Locate every white blood cell.
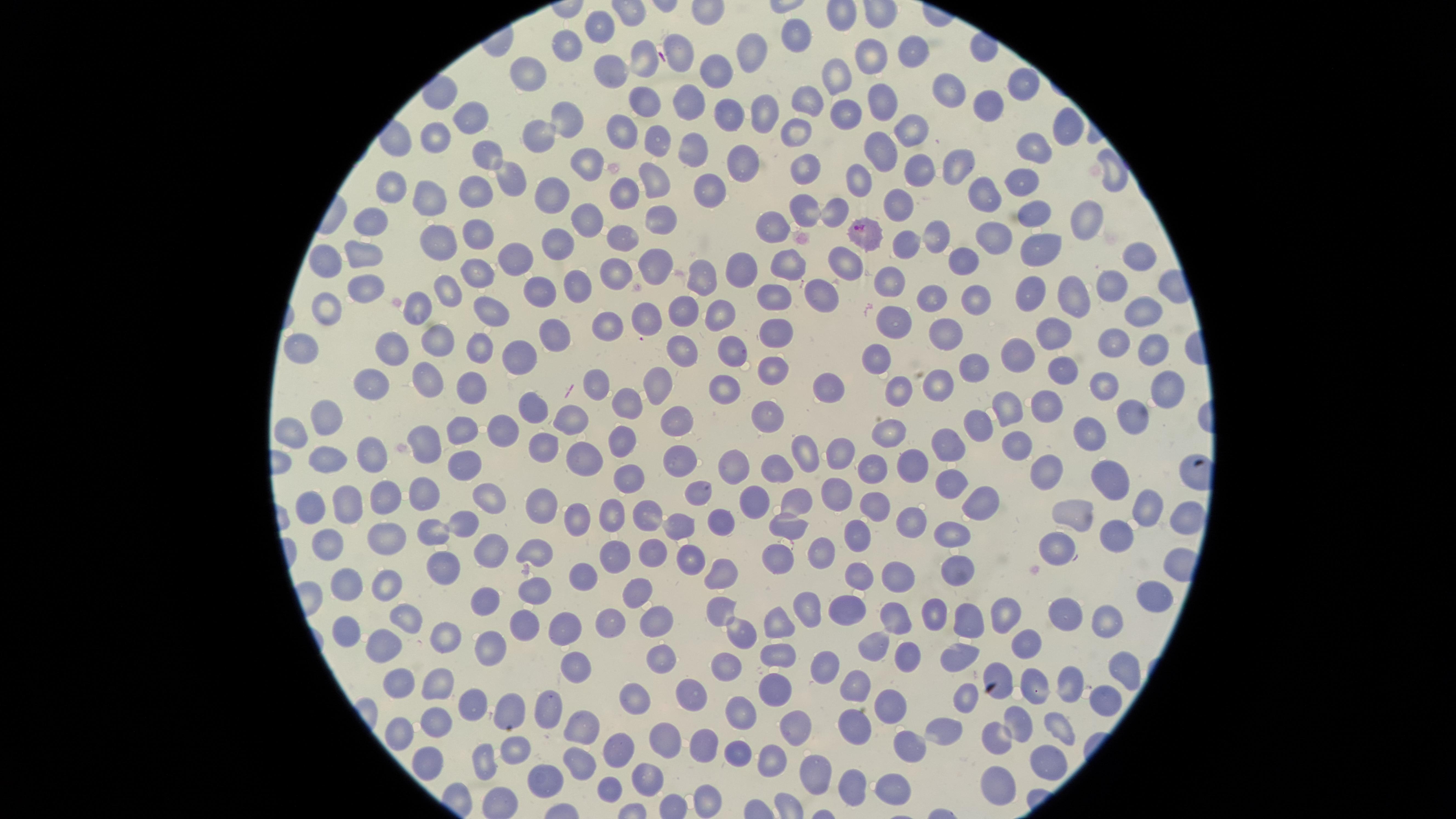
No white blood cells identified.

Approximate marker points as [x, y] in pixels.
Summary:
  - Parasitized red blood cells: [859, 230], [734, 351]
  - Uninfected red blood cells: [603, 29], [799, 32], [571, 44], [910, 50], [747, 54], [681, 55], [870, 55], [642, 57], [527, 69], [612, 70], [712, 72], [841, 73], [1020, 78], [954, 91], [806, 100], [644, 102], [888, 102], [688, 106], [764, 108], [983, 108], [844, 110], [732, 111], [564, 117], [473, 119], [1063, 129], [617, 130], [791, 130], [432, 133], [912, 134], [535, 138], [658, 138], [1036, 143], [694, 151], [488, 154], [876, 154], [738, 160], [584, 161], [956, 164], [808, 170], [918, 170], [1113, 174], [511, 179], [655, 182], [854, 182], [1025, 183], [394, 184], [711, 185], [475, 188], [547, 189], [622, 189], [432, 193], [983, 196], [900, 204], [834, 209], [1032, 209], [807, 212], [372, 213], [583, 216], [661, 221], [1081, 224], [626, 229], [767, 230], [935, 235], [479, 236], [996, 236], [436, 240], [558, 242], [902, 244], [1037, 247], [358, 251], [848, 253], [1137, 253], [326, 255], [966, 257], [513, 259], [789, 266], [653, 267], [743, 268], [614, 269], [476, 275], [698, 277], [582, 282], [888, 285], [1104, 285], [362, 287], [538, 287], [442, 288], [819, 292], [1029, 292], [1074, 296], [931, 297], [765, 298], [973, 301], [1139, 306], [329, 307], [489, 308], [683, 310], [721, 311], [647, 320], [894, 326], [607, 327], [554, 330], [780, 331], [1046, 333], [946, 334], [1112, 337], [435, 338], [685, 343], [302, 345], [394, 346], [477, 346], [1143, 347], [1014, 354], [515, 356], [876, 359], [972, 365], [774, 367], [1068, 371], [426, 380], [726, 380], [936, 380], [595, 381], [656, 381], [377, 383], [827, 383], [1096, 387], [1166, 387], [472, 388], [897, 392], [626, 399], [1042, 399], [1007, 401], [531, 404], [1133, 410], [679, 418], [768, 418], [331, 421], [574, 423], [975, 423], [457, 426], [503, 428], [294, 431], [892, 431], [1088, 435], [429, 440], [616, 443], [957, 446], [1019, 447], [543, 450], [839, 452], [378, 454], [805, 454], [463, 457], [587, 457], [677, 458], [326, 461], [733, 464], [909, 468], [1046, 469], [781, 471], [872, 471], [1112, 476], [628, 478], [960, 482], [485, 489], [694, 491], [423, 492], [802, 494], [841, 495], [385, 496], [754, 498], [982, 499], [348, 501], [877, 504], [543, 505], [1148, 507], [1076, 508], [313, 510], [648, 513], [612, 517], [1186, 518], [914, 519], [683, 520], [462, 523], [722, 523], [782, 526], [434, 529], [575, 529], [949, 531], [1117, 533], [855, 537], [389, 541], [327, 543], [491, 548], [1056, 549], [656, 550], [824, 551], [537, 553], [691, 555], [619, 557], [775, 557], [962, 565], [721, 569], [451, 571], [579, 572], [905, 576], [864, 577], [382, 579], [642, 588], [537, 589], [334, 591], [487, 596], [1150, 597], [851, 605], [808, 606], [714, 608], [1008, 611], [933, 613], [1065, 613], [658, 618], [896, 618], [970, 618], [523, 619], [780, 620], [1108, 620], [613, 623], [405, 624], [565, 625], [340, 631], [740, 633], [449, 638], [874, 643], [1027, 643], [382, 645], [479, 649], [778, 649], [906, 656], [956, 657], [574, 658], [662, 659], [1117, 663], [822, 665], [722, 666], [999, 673], [404, 674], [1026, 679], [775, 686], [858, 686], [441, 687], [1066, 687], [693, 691], [637, 696], [968, 699], [1106, 700], [894, 701], [471, 704], [736, 706], [508, 707], [545, 709], [1018, 717], [437, 718], [794, 723], [1062, 726], [582, 727], [394, 728], [854, 728], [943, 728], [668, 734], [996, 735], [906, 745], [513, 747], [703, 748], [617, 751], [739, 756], [576, 758], [422, 759], [487, 759], [1050, 761], [772, 762], [812, 769], [541, 775], [640, 780], [852, 780], [894, 780], [988, 787], [613, 791], [706, 800]
  - Species: Plasmodium falciparum
  - Image size: 1456×819 pixels
  - Presence: malaria parasites detected
  - Preparation: thin blood film
  - Stain: Giemsa
  - Field of view: single
  - Visible region: circular
  - Capture: smartphone photograph through the microscope eyepiece